Locate every leukocyte (white blood cell).
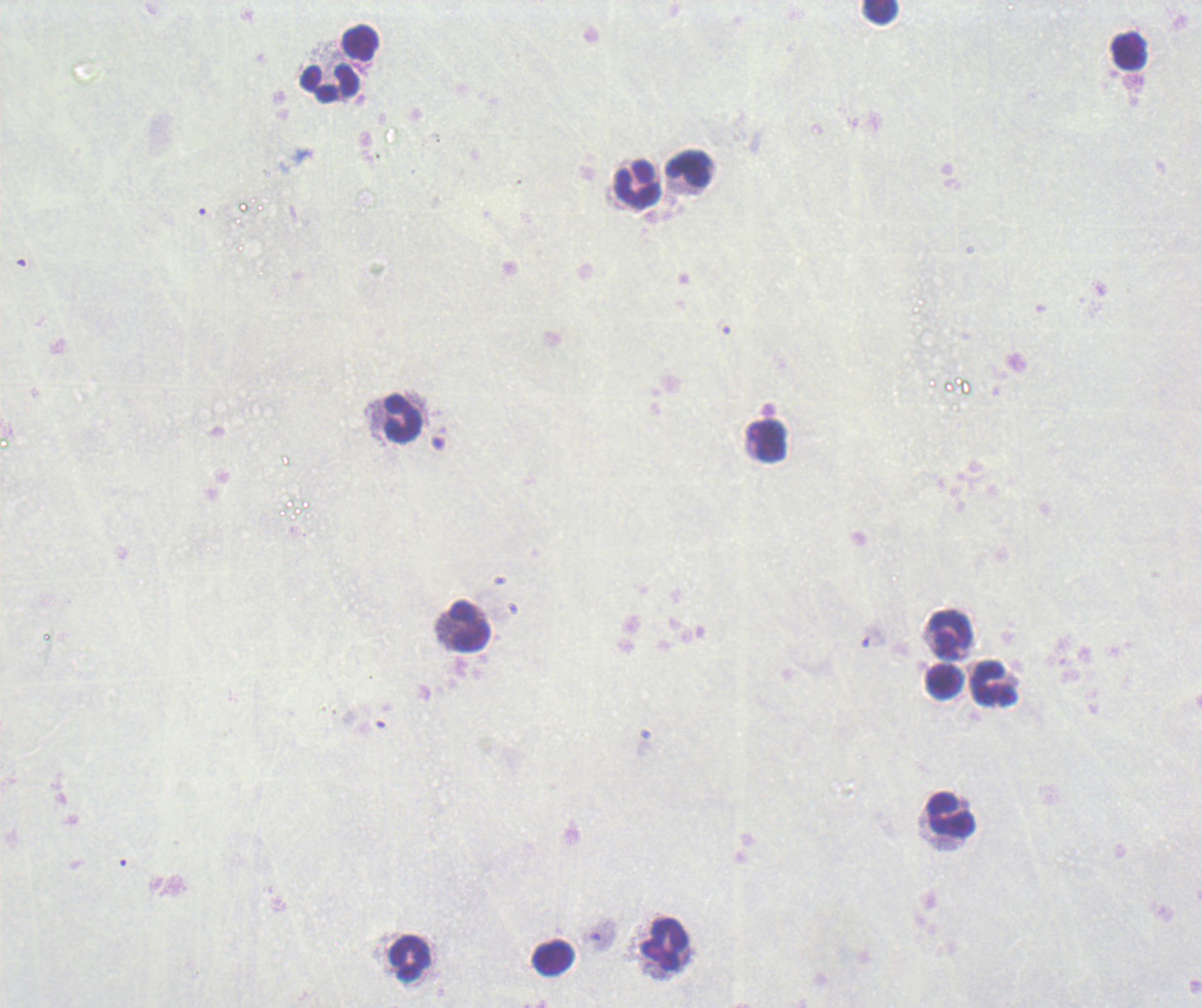
Approximate centers as {x, y} in pixels.
Leukocytes: {881, 12}, {361, 42}, {1129, 54}, {330, 84}, {688, 170}, {638, 186}, {402, 419}, {770, 443}, {470, 627}, {950, 634}, {945, 682}, {994, 684}, {952, 816}, {664, 944}, {411, 958}, {553, 958}.

stain = Romanowsky
context = previously used in an actual diagnosis
preparation = thick smear of blood
image size = 1202×1008 pixels
background quality = unsatisfactory
result = no Plasmodium parasites detected
field of view = single
magnification = 100x